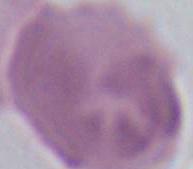
identification = red blood cell
modality = photomicrograph
magnification = 1000x